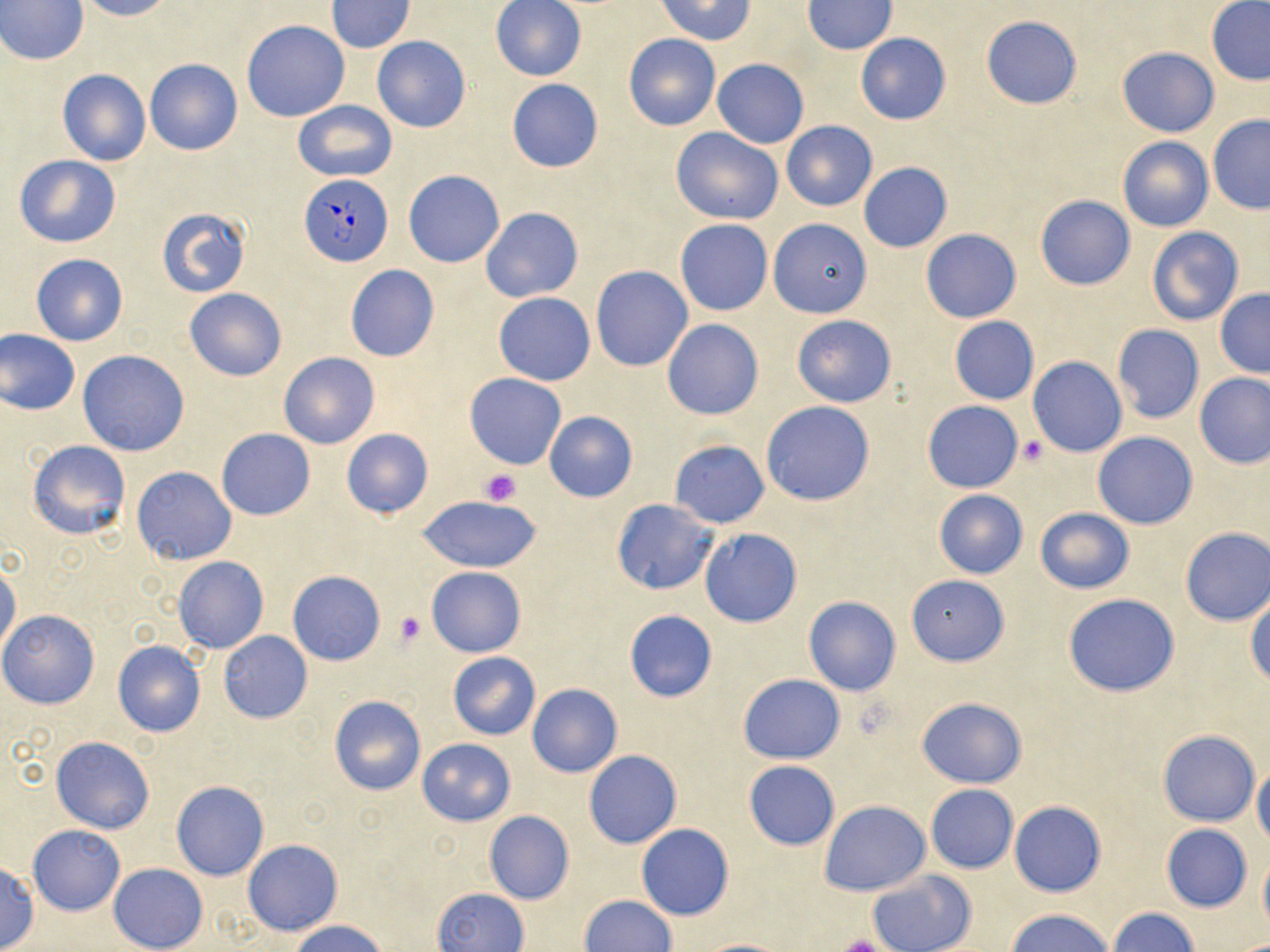

slide_level_diagnosis: Plasmodium falciparum
image_size: 1270×952 pixels
preparation: thin blood smear
plasmodium_falciparum_infected_red_blood_cell_locations: 'approximate bounding boxes as (x1,y1)-(x2,y2) corner pairs in pixels: (298,174)-(395,265)'
field_of_view: one of a larger specimen
uninfected_red_blood_cell_locations: 'approximate bounding boxes as (x1,y1)-(x2,y2) corner pairs in pixels: (77,0)-(172,22), (490,0)-(586,82), (657,0)-(755,44), (1,1)-(88,66), (327,1)-(414,52), (802,1)-(896,54), (1205,1)-(1270,85), (980,15)-(1082,109), (241,20)-(349,122), (856,33)-(951,125), (624,35)-(720,131), (372,36)-(470,132), (1116,47)-(1220,137), (146,59)-(242,155), (712,59)-(809,149), (58,68)-(151,166), (506,79)-(603,172), (293,100)-(397,183), (1207,115)-(1270,213), (781,120)-(877,212), (670,128)-(783,226), (1117,136)-(1213,233), (14,155)-(122,248), (858,162)-(952,252), (404,170)-(504,267), (1035,195)-(1135,290), (481,207)-(583,303), (157,208)-(251,297), (768,218)-(872,318), (675,219)-(774,316), (1147,226)-(1243,326), (920,229)-(1022,323), (31,254)-(128,345), (345,265)-(439,361), (591,265)-(692,371), (184,288)-(287,382), (1214,289)-(1270,379), (494,293)-(595,385), (791,315)-(896,407), (949,316)-(1039,405), (662,319)-(763,419), (1111,325)-(1205,424), (0,328)-(80,415), (77,350)-(190,456), (277,352)-(380,449), (1027,357)-(1126,458), (1194,372)-(1270,469), (465,373)-(567,468), (921,400)-(1024,493), (761,401)-(874,506), (544,412)-(637,502), (216,429)-(315,519), (341,429)-(433,520), (1093,431)-(1198,529), (27,439)-(131,540), (670,439)-(769,528), (130,466)-(236,564), (933,491)-(1027,578), (416,495)-(545,573), (610,498)-(719,594), (1036,507)-(1135,594), (1180,527)-(1270,626), (699,528)-(802,627), (173,556)-(269,654), (0,561)-(19,659), (427,566)-(526,658), (287,571)-(386,666), (906,575)-(1009,666), (1063,594)-(1180,696), (1246,594)-(1270,688), (803,596)-(901,696), (624,610)-(717,703), (0,611)-(100,709), (217,630)-(312,724), (113,640)-(206,737), (448,652)-(540,740), (737,673)-(845,764), (527,683)-(622,778), (328,695)-(426,796), (915,696)-(1027,788), (1157,730)-(1259,826), (51,736)-(155,834), (417,738)-(515,826), (584,749)-(682,849), (742,760)-(841,851), (1252,764)-(1270,845), (171,780)-(269,880), (926,785)-(1018,873), (820,800)-(930,896), (1010,800)-(1106,897), (484,811)-(574,905), (636,823)-(734,921), (1161,824)-(1252,912), (28,825)-(125,915), (244,839)-(343,936), (1258,853)-(1270,934), (0,861)-(37,951), (108,863)-(207,952), (866,870)-(975,952), (435,888)-(528,952), (580,895)-(676,952), (1108,908)-(1198,952), (1005,909)-(1115,952), (289,920)-(389,952), (695,938)-(795,952)'
platelet_locations: 'approximate bounding boxes as (x1,y1)-(x2,y2) corner pairs in pixels: (1017,436)-(1048,466), (481,470)-(522,505), (395,612)-(425,645), (831,937)-(894,952)'
magnification: 1000x
modality: optical microscopy
stain: May-Grünwald-Giemsa